Point out each malaria parasite and each leukocyte.
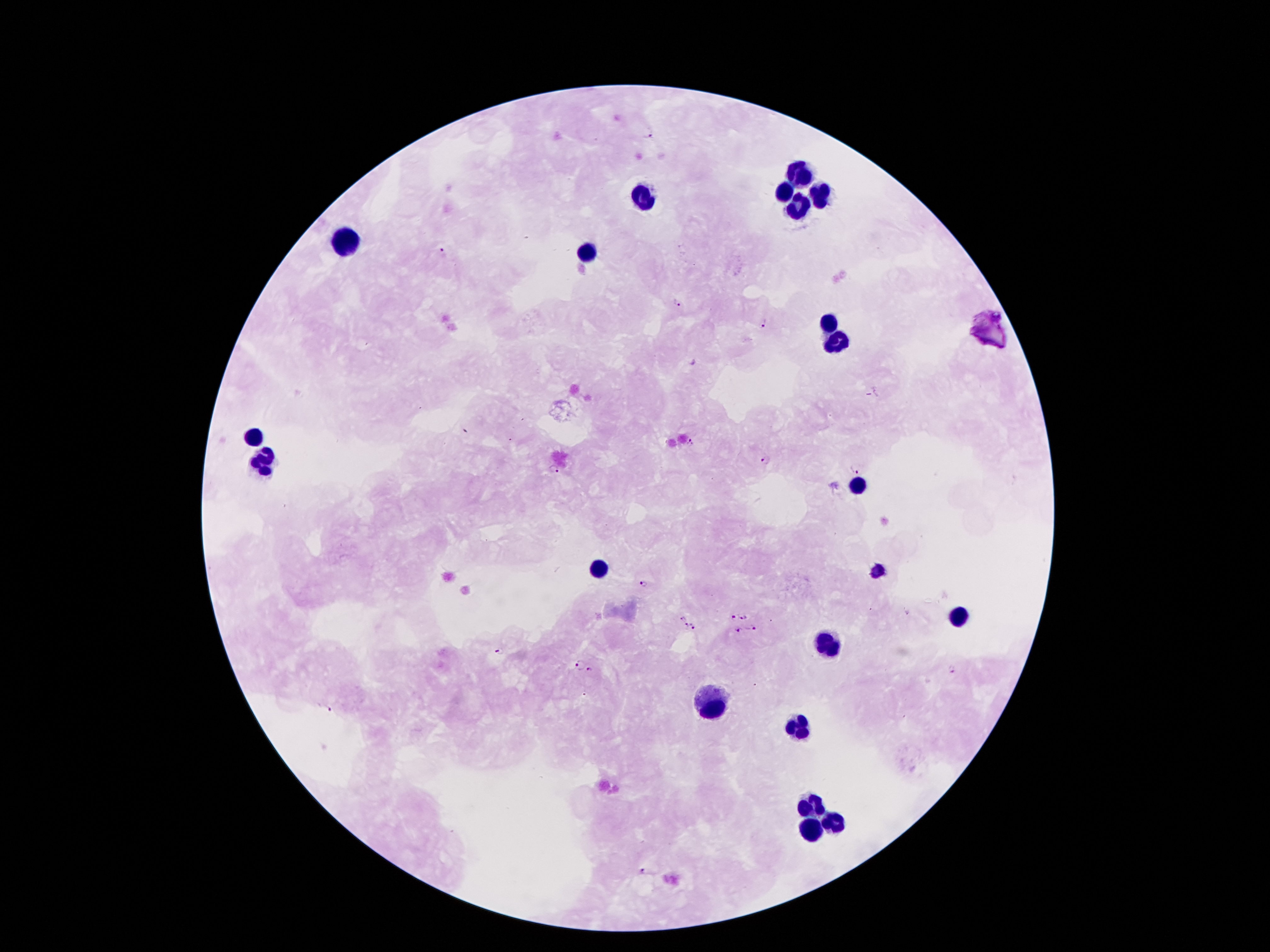
Approximate centers as {x, y} in pixels.
Malaria parasites: {647, 133}, {441, 251}, {677, 302}, {763, 324}, {691, 441}, {764, 461}, {553, 468}, {855, 468}, {644, 582}, {734, 616}, {682, 617}, {743, 617}, {686, 625}, {692, 625}, {754, 628}, {738, 629}, {501, 651}, {581, 664}, {590, 669}, {951, 669}, {327, 707}, {644, 871}.
Leukocytes: {798, 168}, {785, 191}, {646, 194}, {817, 197}, {796, 210}, {350, 240}, {590, 252}, {827, 323}, {838, 342}, {252, 437}, {264, 458}, {858, 484}, {601, 566}, {877, 571}, {955, 617}, {823, 643}, {712, 702}, {801, 725}, {813, 805}, {835, 824}, {811, 828}.

image size = 1270×952 pixels
field of view = single
preparation = thick blood film
capture = smartphone through the microscope eyepiece
patient malaria status = positive for Plasmodium falciparum
stain = Giemsa
magnification = 100x